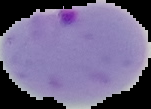

From a thin blood smear. Result: malaria parasites detected. Image is 151×109 pixels. Cell region segmented out of the field of view; the surrounding area is masked to black.